Give the position of every leukocyte visible.
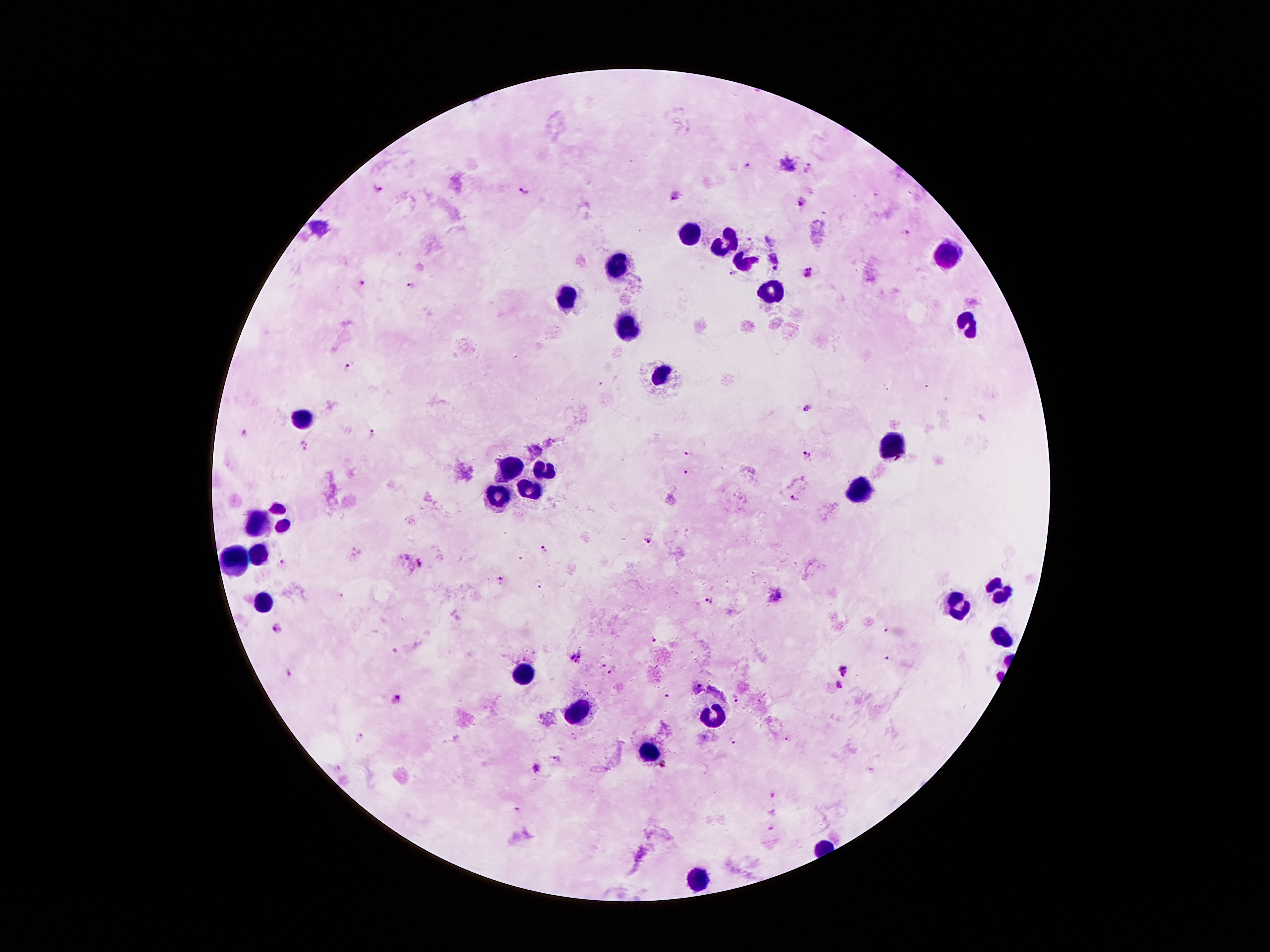
Approximate centers as (x, y) in pixels.
Leukocytes: (692, 235), (728, 242), (946, 250), (744, 259), (618, 261), (770, 290), (566, 299), (969, 322), (625, 325), (656, 374), (303, 421), (892, 445), (540, 468), (508, 470), (859, 486), (496, 492), (530, 494), (285, 515), (257, 522), (257, 555), (234, 560), (995, 583), (957, 602), (263, 604), (1001, 635), (518, 674), (579, 712), (717, 719), (648, 747), (697, 877).

Malaria parasite locations: (748, 166), (809, 167), (378, 188), (523, 191), (672, 193), (803, 202), (906, 234), (768, 239), (750, 242), (777, 261), (732, 272), (810, 273), (361, 283), (411, 285), (348, 366), (600, 383), (807, 409), (373, 432), (244, 433), (305, 446), (689, 453), (807, 454), (686, 472), (796, 499), (648, 540), (543, 548), (282, 563), (418, 563), (500, 581), (538, 584), (774, 593), (712, 601), (278, 630), (654, 640), (576, 657), (600, 665), (845, 668), (613, 672), (289, 676), (837, 685), (667, 696), (736, 698), (395, 699), (360, 737), (787, 739), (734, 742), (558, 757), (537, 767), (666, 767), (771, 794), (518, 810), (772, 811), (771, 829). 100x magnification. Giemsa stain. Single field of view. Thick peripheral-blood smear. Image is 1270×952 pixels. Photographed through the microscope eyepiece with a smartphone camera. Patient malaria status: positive for Plasmodium falciparum.